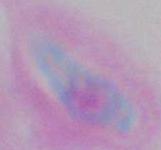
magnification: 1000x
identification: Toxoplasma gondii
modality: micrograph